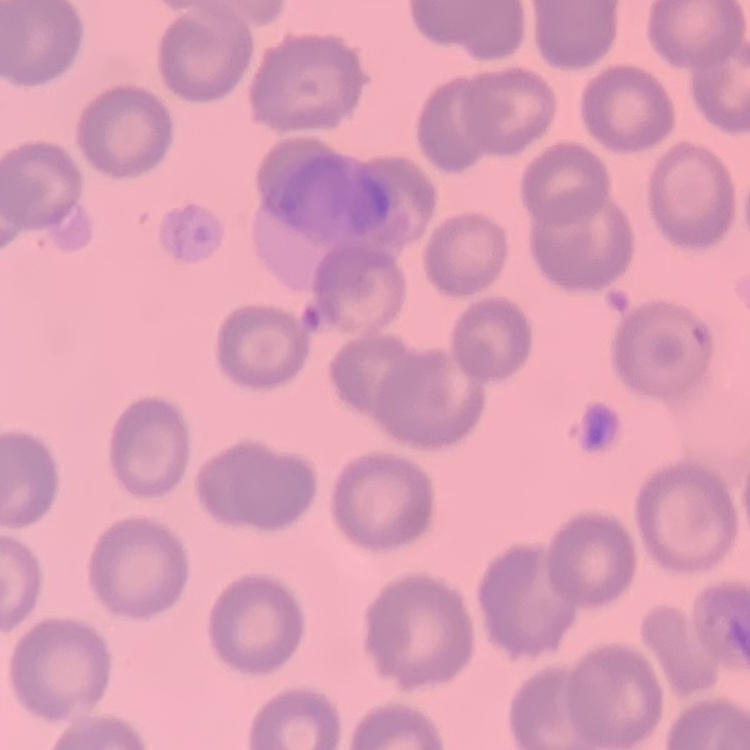
Summary:
  - Red blood cell morphology: no rouleaux formation
  - Preparation: thin peripheral smear
  - Image type: square crop of a larger photomicrograph
  - Stain: Field's or Giemsa